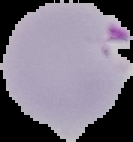 Image is 133×142 pixels. Malaria status: parasitized. From a thin blood film. Segmented cell region on a black background.